Name the cell type shown.
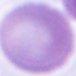
This is an erythrocyte.

modality: photomicrograph
magnification: 1000x